Locate every blood parasite and identify its species.
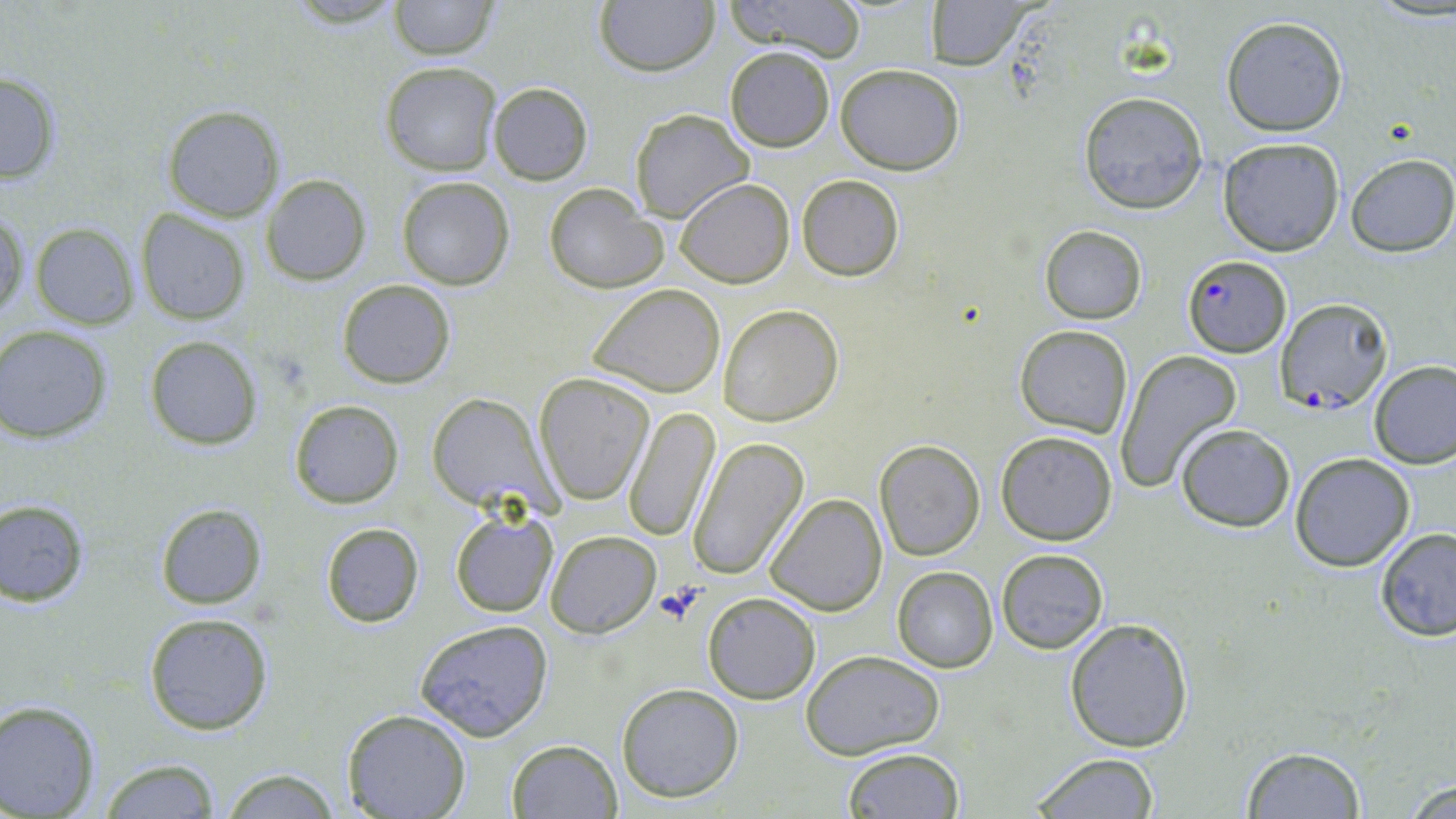

Approximate bounding boxes as named x1/y1/x2/y2 corners in pixels.
Plasmodium falciparum-infected red blood cells: (x1=1182, y1=256, x2=1293, y2=356), (x1=1276, y1=296, x2=1391, y2=414).
No Plasmodium ovale, Plasmodium malariae, Plasmodium vivax, Babesia divergens, or Trypanosoma brucei observed.

Platelet locations: (x1=1380, y1=116, x2=1418, y2=148), (x1=655, y1=583, x2=706, y2=625). Uninfected red blood cell locations: (x1=720, y1=0, x2=870, y2=62), (x1=388, y1=1, x2=497, y2=60), (x1=595, y1=1, x2=718, y2=75), (x1=923, y1=1, x2=1036, y2=71), (x1=1220, y1=17, x2=1348, y2=136), (x1=724, y1=46, x2=836, y2=152), (x1=381, y1=61, x2=502, y2=176), (x1=835, y1=63, x2=965, y2=173), (x1=0, y1=70, x2=64, y2=184), (x1=487, y1=81, x2=594, y2=185), (x1=1077, y1=92, x2=1209, y2=213), (x1=161, y1=104, x2=284, y2=223), (x1=629, y1=109, x2=752, y2=222), (x1=1218, y1=137, x2=1347, y2=257), (x1=1346, y1=153, x2=1456, y2=257), (x1=262, y1=174, x2=370, y2=284), (x1=796, y1=175, x2=904, y2=280), (x1=396, y1=176, x2=515, y2=290), (x1=675, y1=176, x2=794, y2=288), (x1=544, y1=184, x2=665, y2=294), (x1=1, y1=205, x2=28, y2=322), (x1=135, y1=209, x2=252, y2=324), (x1=29, y1=222, x2=138, y2=329), (x1=1039, y1=225, x2=1146, y2=324), (x1=337, y1=278, x2=455, y2=388), (x1=590, y1=283, x2=726, y2=398), (x1=720, y1=304, x2=842, y2=426), (x1=0, y1=325, x2=114, y2=444), (x1=1016, y1=325, x2=1133, y2=436), (x1=144, y1=336, x2=262, y2=450), (x1=1115, y1=349, x2=1243, y2=491), (x1=1370, y1=360, x2=1456, y2=469), (x1=532, y1=372, x2=654, y2=506), (x1=427, y1=393, x2=550, y2=512), (x1=289, y1=398, x2=405, y2=509), (x1=623, y1=404, x2=720, y2=542), (x1=1174, y1=424, x2=1294, y2=531), (x1=996, y1=429, x2=1118, y2=545), (x1=687, y1=435, x2=810, y2=580), (x1=873, y1=439, x2=986, y2=561), (x1=1289, y1=453, x2=1414, y2=572), (x1=764, y1=492, x2=888, y2=615), (x1=0, y1=500, x2=90, y2=606), (x1=155, y1=502, x2=268, y2=609), (x1=449, y1=511, x2=559, y2=617), (x1=320, y1=522, x2=423, y2=626), (x1=1375, y1=529, x2=1456, y2=641), (x1=547, y1=530, x2=660, y2=638), (x1=996, y1=547, x2=1109, y2=655), (x1=891, y1=567, x2=997, y2=673), (x1=703, y1=593, x2=820, y2=704), (x1=142, y1=612, x2=274, y2=735), (x1=1064, y1=617, x2=1193, y2=753), (x1=414, y1=618, x2=555, y2=740), (x1=800, y1=648, x2=947, y2=761), (x1=617, y1=682, x2=744, y2=803), (x1=0, y1=700, x2=101, y2=818), (x1=342, y1=710, x2=472, y2=819), (x1=507, y1=739, x2=621, y2=819), (x1=1242, y1=746, x2=1365, y2=817), (x1=842, y1=747, x2=964, y2=818), (x1=1028, y1=752, x2=1161, y2=819), (x1=97, y1=760, x2=222, y2=818), (x1=215, y1=767, x2=344, y2=818), (x1=1397, y1=777, x2=1456, y2=818). Slide-level diagnosis: Plasmodium falciparum. One field of a larger specimen. Image is 1456×819 pixels. Thin blood film. Optical microscopy. May-Grünwald-Giemsa stain. 1000x magnification.